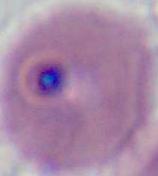
Summary:
  - Modality: micrograph
  - Identification: Plasmodium
  - Magnification: 400x or 1000x